Outline each P. falciparum parasite and classify it by life-cycle stage.
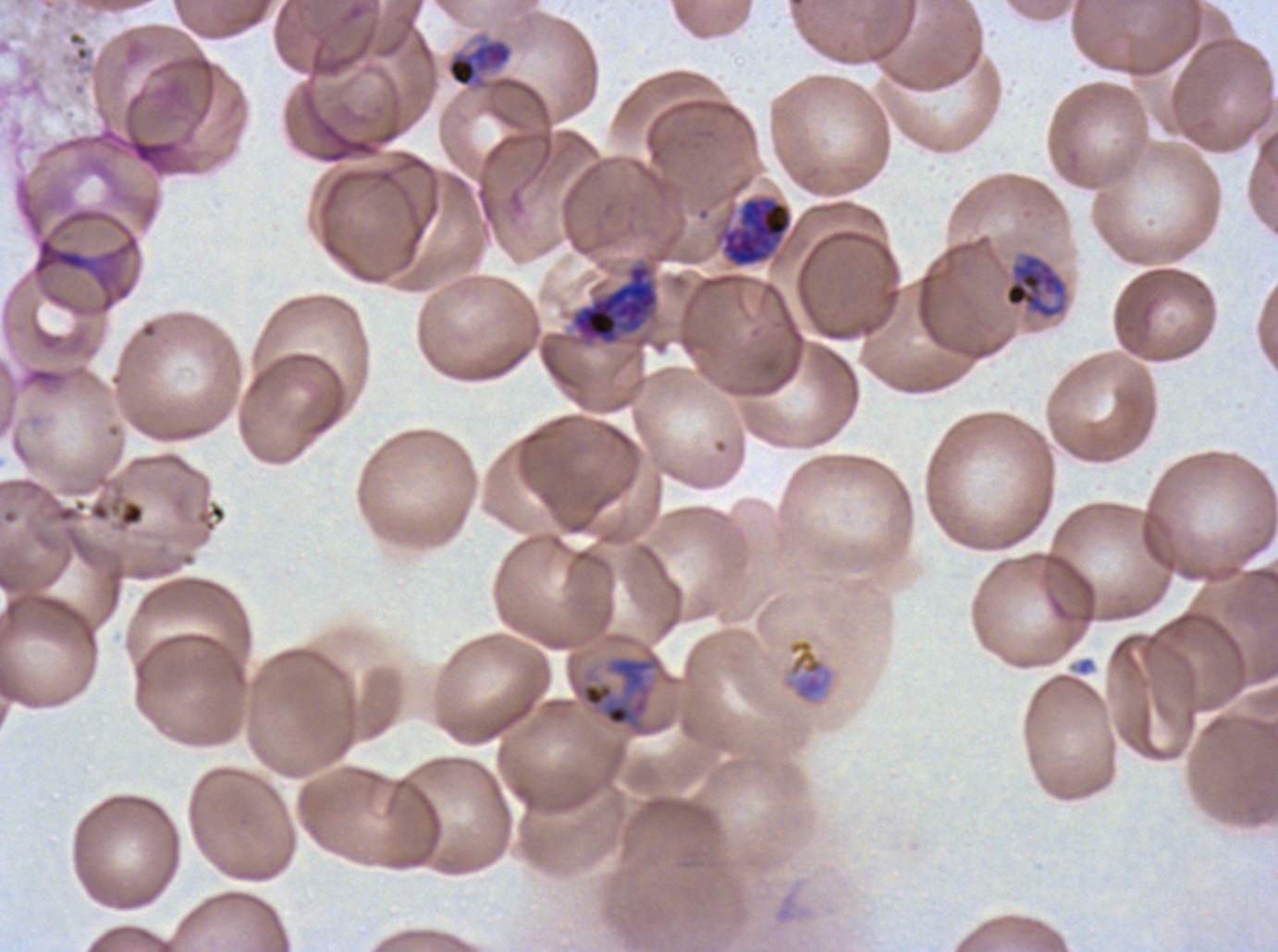

Approximate bounding rectangles given as corner coordinates in pixels from the top-left.
Late-ring/early-trophozoite forms: (x1=447, y1=41, x2=511, y2=87).
Mid trophozoites: (x1=783, y1=638, x2=834, y2=703).
Late trophozoites: (x1=1004, y1=252, x2=1068, y2=320), (x1=581, y1=656, x2=655, y2=729).
Early schizonts: (x1=570, y1=261, x2=660, y2=348).
Late schizonts: (x1=714, y1=194, x2=793, y2=269).
No rings, segmenters, or gametocytes observed.

Summary:
  - Debris locations: (x1=119, y1=501, x2=144, y2=526)
  - Field of view: one sub-image of a larger composite
  - Specimen: ex-vivo P. falciparum culture from a patient in The Gambia, grown for 24 to 48 hours
  - Image size: 1278×952 pixels
  - Stain: Giemsa
  - Life-cycle stages observed: late-ring/early-trophozoite, mid trophozoite, late trophozoite, early schizont, late schizont
  - Preparation: thin blood film